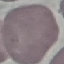

Summary:
  - Malaria status: uninfected
  - Image type: automatically extracted cell patch, resized to 64 × 64 pixels
  - Stain: Giemsa
  - Capture: smartphone through the microscope eyepiece
  - Preparation: thin blood smear